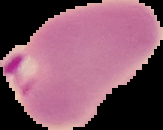
{
  "preparation": "thin blood film",
  "image_size": "163×130 pixels",
  "image_type": "cell region segmented out of the field of view; surrounding area masked to black",
  "malaria_status": "parasitized"
}